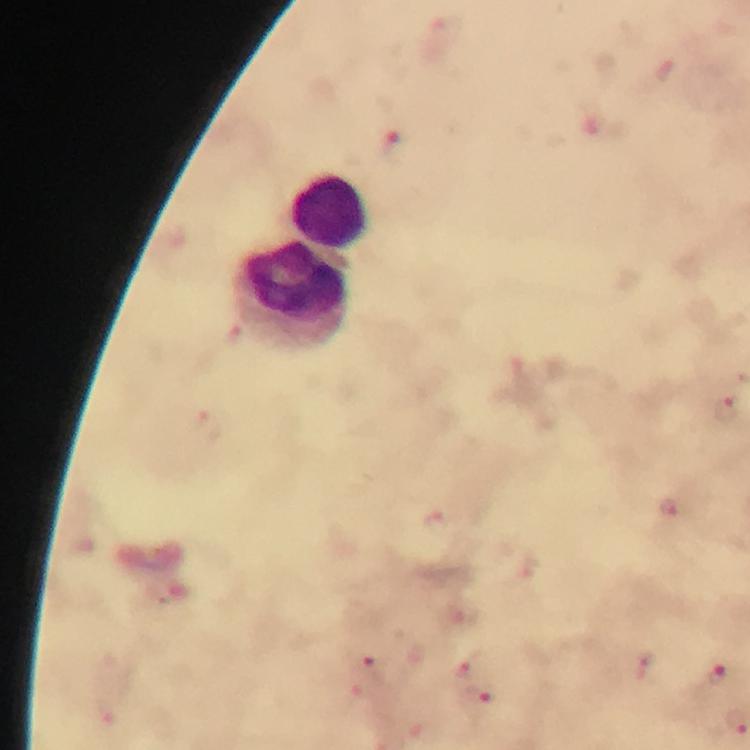
Approximate centers as [x, y] in pixels. Leukocyte locations: [328, 210], [293, 294]. Plasmodium parasite locations: [727, 408], [460, 619], [646, 664], [470, 665], [374, 666], [718, 674], [477, 702]. Giemsa stain. Immersion oil applied. Cropped region of a single field of view. Photographed through the microscope with a smartphone camera. At 100x magnification. Image is 750×750 pixels. From a diagnostic examination for malaria. Thick smear.